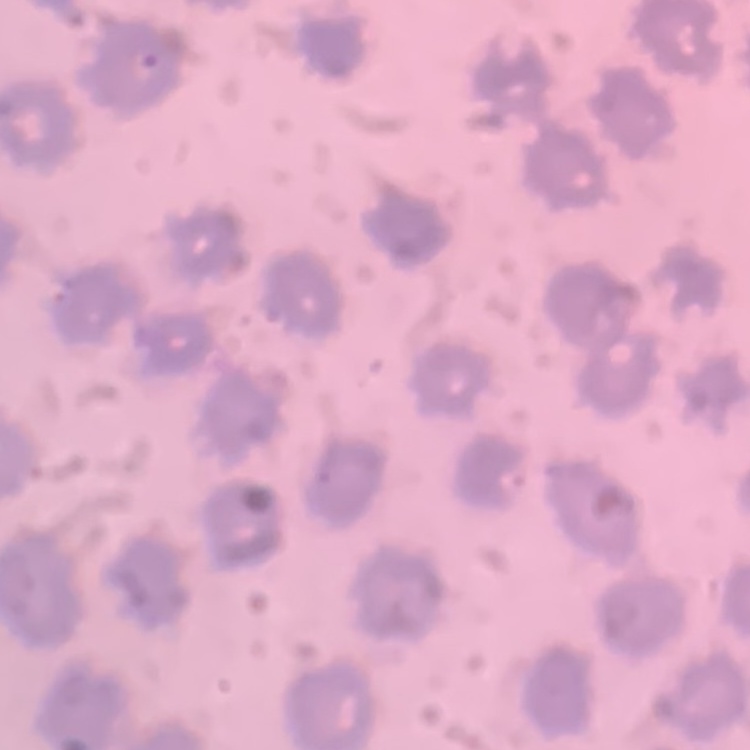 The red blood cells show no rouleaux formation. Stained with either Field's or Giemsa. Thin blood smear. One tile cut from a larger photomicrograph.